Locate every Plasmodium parasite.
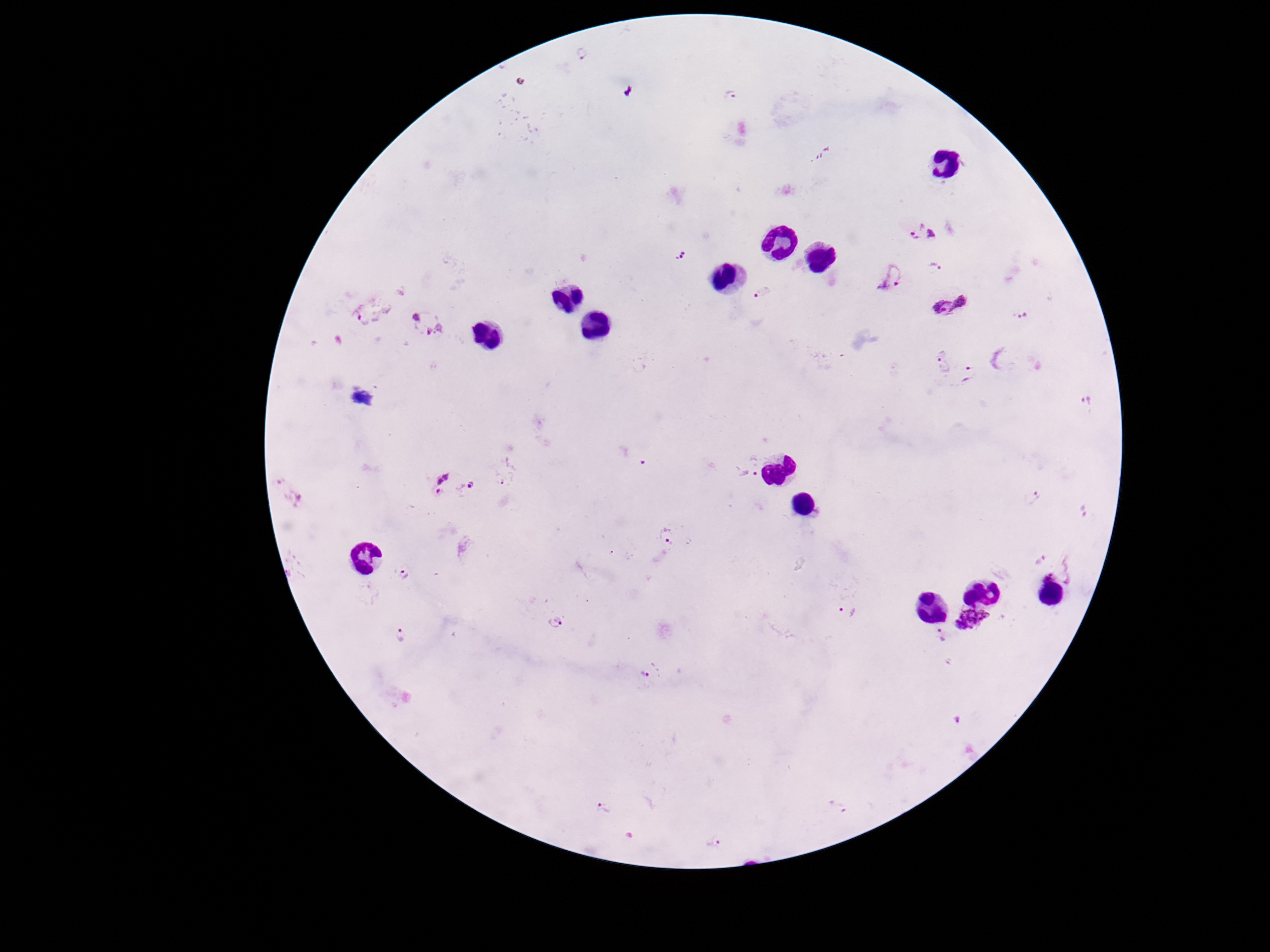
Approximate centers as [x, y] in pixels.
Plasmodium parasites: [583, 55], [729, 95], [910, 232], [932, 235], [679, 255], [936, 267], [891, 277], [762, 291], [948, 306], [369, 311], [1023, 314], [425, 322], [940, 362], [970, 372], [1085, 401], [746, 474], [276, 481], [441, 482], [471, 485], [1033, 496], [298, 501], [1082, 511], [666, 535], [1042, 560], [1068, 572], [405, 575], [1045, 578], [848, 611], [970, 618], [555, 622], [940, 635], [401, 636], [645, 673], [958, 720], [837, 807], [603, 808], [714, 843].

One field from this slide. Image is 1270×952 pixels. Patient malaria status: infected. Smartphone photograph taken through the microscope eyepiece. 100x magnification. Giemsa-stained preparation. Thick peripheral-blood smear.